Classify this cell by malaria status.
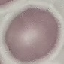

It is uninfected.

{
  "stain": "Giemsa",
  "capture": "smartphone camera at the microscope eyepiece",
  "image_type": "cell patch, automatically extracted from a larger field of view and resized to 64 × 64 pixels",
  "preparation": "thin blood film"
}